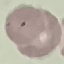
Summary:
  - Result: malaria parasites detected
  - Stain: Giemsa
  - Image type: cell patch, automatically extracted from a larger field of view and resized to 64 × 64 pixels
  - Preparation: thin blood film
  - Capture: smartphone through the microscope eyepiece